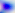

magnification = 400x
identification = Toxoplasma gondii
modality = micrograph